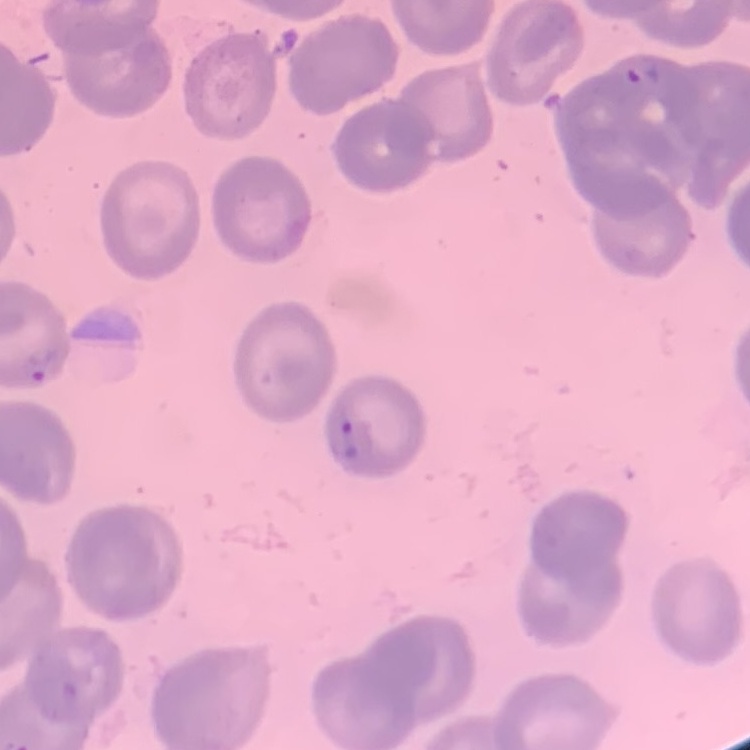
Summary:
  - Erythrocyte morphology: no rouleaux formation
  - Stain: Field's or Giemsa
  - Preparation: thin blood film
  - Image type: one tile cut from a larger photomicrograph